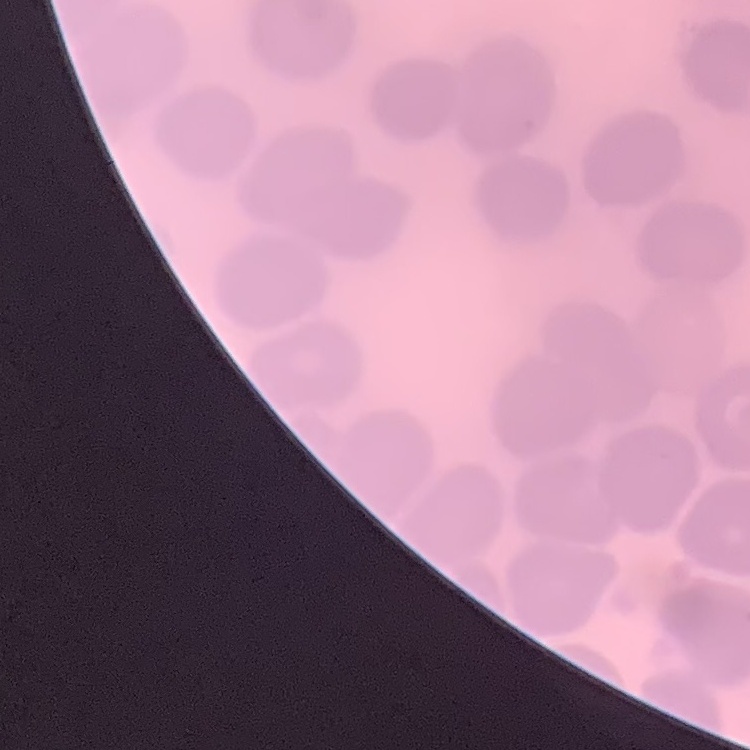
Summary:
  - Erythrocyte morphology: no rouleaux formation
  - Image type: square crop of a larger photomicrograph
  - Stain: Field's or Giemsa
  - Preparation: thin blood smear